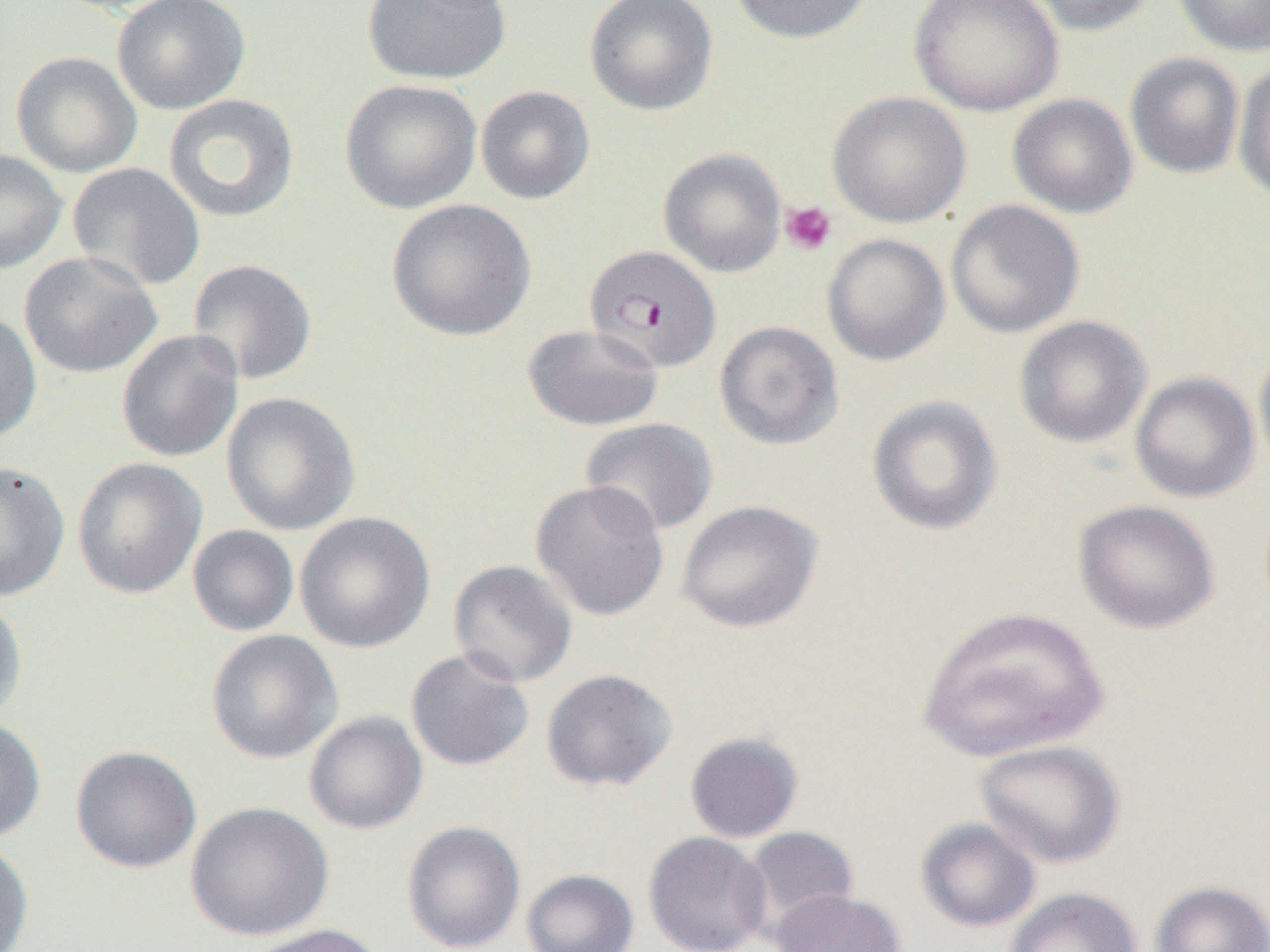

Approximate bounding boxes as (x1,y1)-(x2,y2) corner pairs in pixels. Platelet locations: (780,200)-(837,255). Uninfected red blood cell locations: (112,0)-(251,115), (360,0)-(512,85), (584,0)-(719,116), (730,0)-(872,44), (910,0)-(1063,116), (1016,0)-(1156,36), (1171,0)-(1270,57), (48,1)-(188,16), (10,50)-(143,177), (1124,52)-(1245,179), (1233,57)-(1270,202), (339,79)-(482,215), (475,85)-(596,205), (827,91)-(972,229), (1007,92)-(1138,219), (162,93)-(301,223), (0,147)-(68,275), (658,147)-(786,277), (67,162)-(206,291), (386,199)-(537,342), (945,199)-(1085,338), (821,233)-(950,366), (19,251)-(163,379), (187,258)-(318,385), (0,309)-(43,443), (1013,315)-(1152,448), (714,320)-(844,450), (522,323)-(664,430), (116,330)-(244,463), (1254,341)-(1270,481), (1130,370)-(1260,503), (221,391)-(361,536), (866,395)-(1004,536), (580,417)-(719,536), (72,457)-(206,599), (0,460)-(70,602), (529,480)-(670,621), (676,499)-(823,633), (1072,499)-(1220,633), (294,511)-(435,653), (187,525)-(299,637), (447,559)-(578,687), (0,595)-(28,725), (915,606)-(1110,762), (206,629)-(344,763), (405,648)-(535,771), (541,668)-(678,791), (304,711)-(428,835), (0,716)-(46,845), (684,731)-(803,842), (974,739)-(1126,869), (70,745)-(202,873), (185,801)-(334,941), (916,817)-(1042,933), (402,820)-(526,952), (740,826)-(859,941), (644,831)-(771,952), (0,838)-(34,952), (521,869)-(639,952), (1151,880)-(1270,952), (1003,887)-(1142,951), (772,889)-(906,952), (243,923)-(387,952). Plasmodium falciparum-infected red blood cell locations: (584,244)-(722,373). Slide-level diagnosis: Plasmodium falciparum. Image is 1270×952 pixels. Captured at 1000x magnification. Thin blood smear. Optical microscopy. One field of a larger specimen.